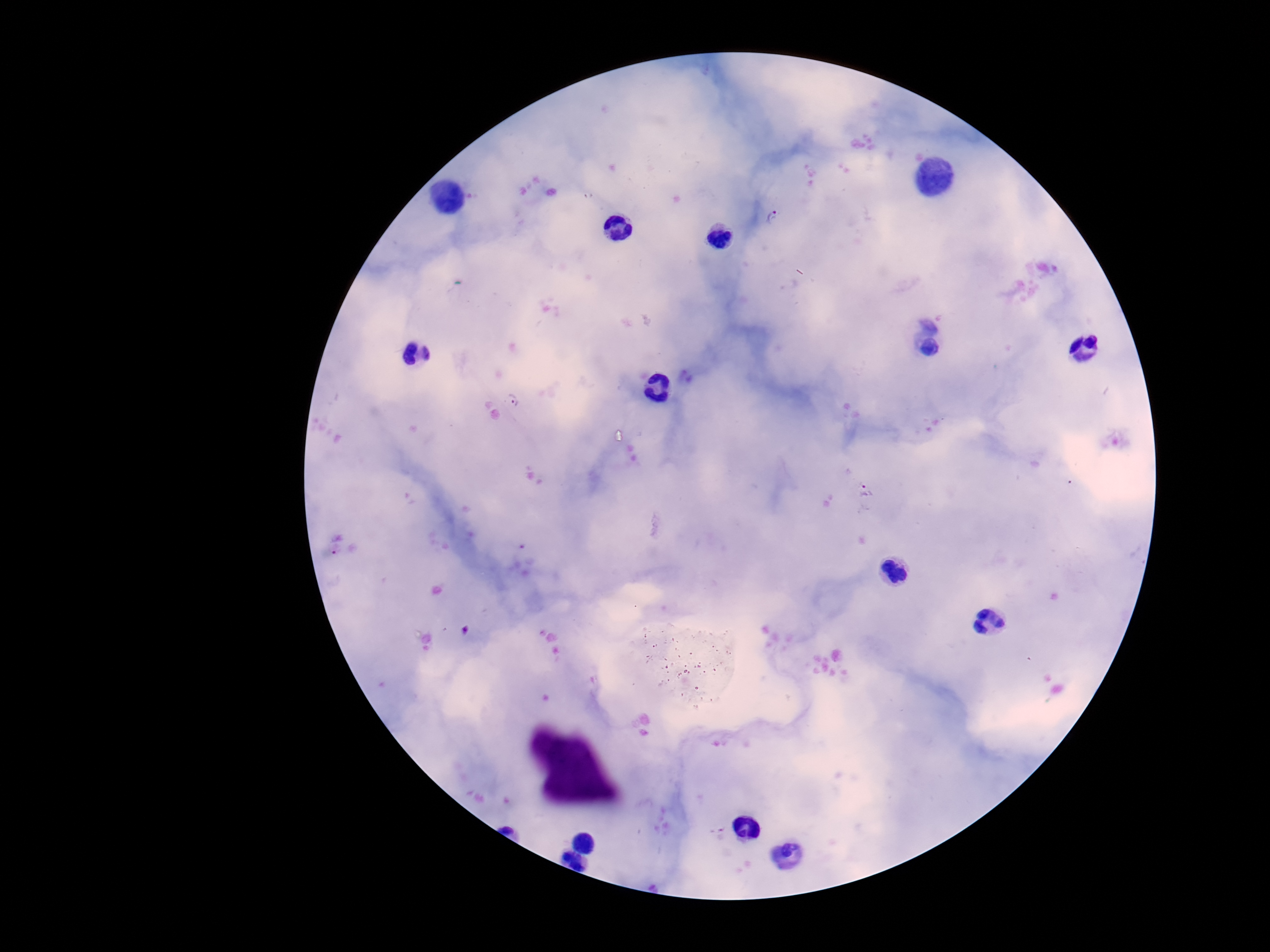

Approximate centers as {x, y} in pixels. Plasmodium parasite locations: {773, 217}, {512, 400}, {865, 490}. Smartphone photograph taken through the microscope eyepiece. Patient malaria status: infected. Thick peripheral-blood smear. 100x magnification. Giemsa-stained preparation. Image is 1270×952 pixels. One field from this slide.